Locate and identify every blood parasite.
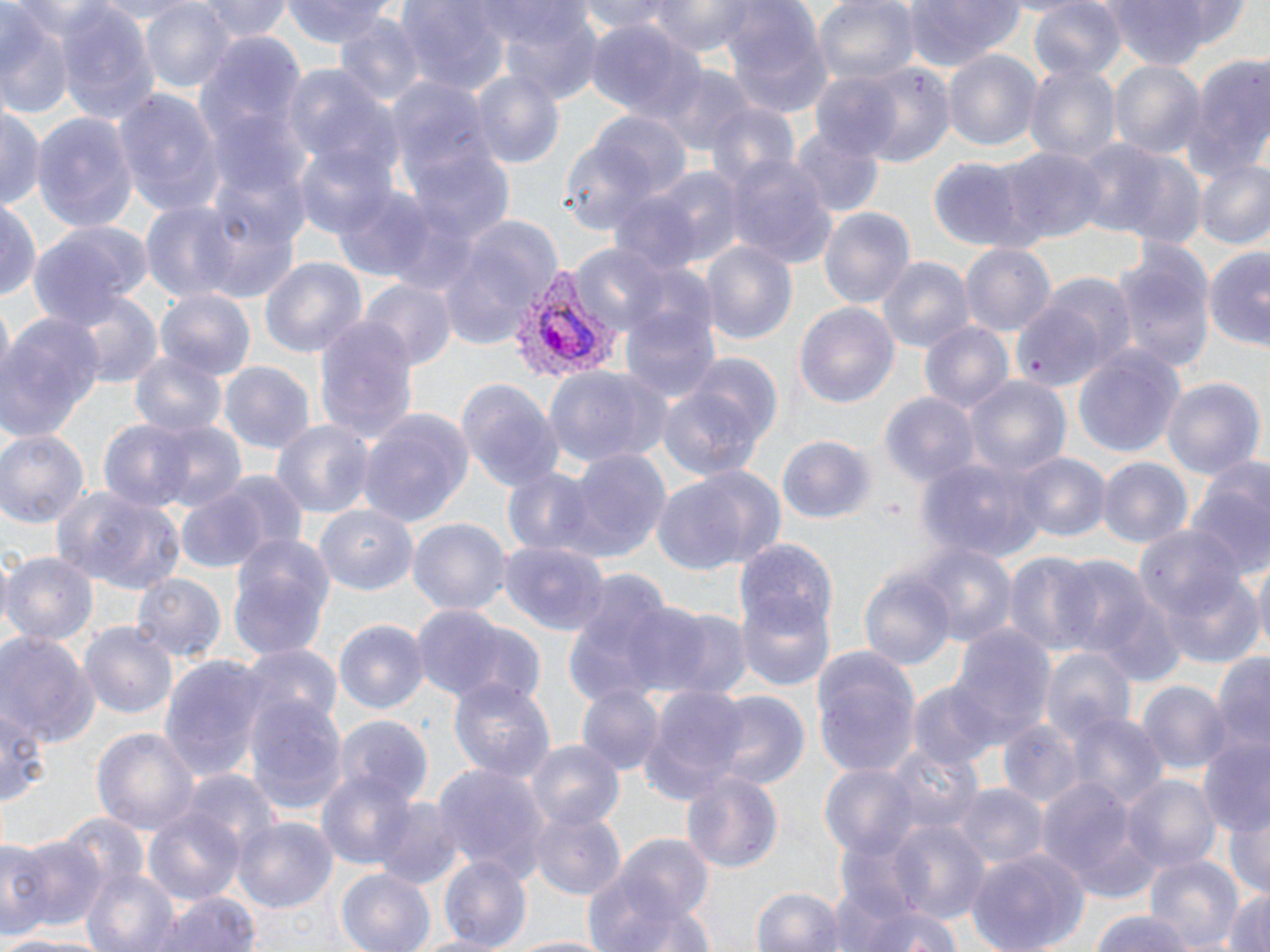

Approximate bounding boxes as named x1/y1/x2/y2 corners in pixels.
Plasmodium vivax-infected red blood cells: (x1=508, y1=266, x2=624, y2=389).
No Plasmodium falciparum, Plasmodium ovale, Plasmodium malariae, Babesia divergens, or Trypanosoma brucei observed.

slide-level diagnosis = Plasmodium vivax
uninfected red blood cell locations = approximate bounding boxes as named x1/y1/x2/y2 corners in pixels: (x1=138, y1=0, x2=231, y2=92), (x1=199, y1=0, x2=291, y2=42), (x1=283, y1=0, x2=399, y2=48), (x1=577, y1=0, x2=679, y2=36), (x1=647, y1=0, x2=761, y2=55), (x1=813, y1=0, x2=918, y2=87), (x1=898, y1=0, x2=1026, y2=70), (x1=1028, y1=1, x2=1127, y2=84), (x1=1095, y1=1, x2=1239, y2=69), (x1=401, y1=2, x2=507, y2=97), (x1=57, y1=3, x2=159, y2=127), (x1=719, y1=5, x2=832, y2=116), (x1=0, y1=7, x2=76, y2=118), (x1=496, y1=7, x2=603, y2=104), (x1=334, y1=15, x2=429, y2=104), (x1=584, y1=19, x2=702, y2=126), (x1=942, y1=49, x2=1044, y2=155), (x1=1182, y1=54, x2=1270, y2=182), (x1=1024, y1=60, x2=1120, y2=166), (x1=1108, y1=61, x2=1204, y2=161), (x1=839, y1=63, x2=957, y2=169), (x1=281, y1=65, x2=401, y2=191), (x1=656, y1=65, x2=755, y2=157), (x1=470, y1=70, x2=565, y2=173), (x1=387, y1=79, x2=493, y2=195), (x1=114, y1=88, x2=224, y2=220), (x1=703, y1=101, x2=803, y2=197), (x1=0, y1=102, x2=44, y2=214), (x1=32, y1=112, x2=139, y2=234), (x1=554, y1=120, x2=675, y2=240), (x1=790, y1=127, x2=884, y2=219), (x1=1071, y1=140, x2=1170, y2=235), (x1=996, y1=145, x2=1106, y2=245), (x1=295, y1=146, x2=395, y2=240), (x1=1097, y1=147, x2=1209, y2=249), (x1=411, y1=149, x2=515, y2=245), (x1=726, y1=157, x2=837, y2=266), (x1=928, y1=159, x2=1030, y2=249), (x1=1192, y1=159, x2=1270, y2=251), (x1=643, y1=167, x2=744, y2=269), (x1=608, y1=187, x2=711, y2=278), (x1=336, y1=189, x2=430, y2=279), (x1=190, y1=192, x2=303, y2=304), (x1=0, y1=198, x2=41, y2=307), (x1=135, y1=199, x2=250, y2=304), (x1=817, y1=206, x2=916, y2=310), (x1=440, y1=213, x2=562, y2=348), (x1=26, y1=220, x2=151, y2=323), (x1=1106, y1=240, x2=1215, y2=374), (x1=700, y1=241, x2=799, y2=350), (x1=961, y1=243, x2=1056, y2=337), (x1=1203, y1=243, x2=1270, y2=353), (x1=572, y1=244, x2=668, y2=332), (x1=877, y1=255, x2=975, y2=355), (x1=258, y1=258, x2=366, y2=363), (x1=1019, y1=271, x2=1138, y2=383), (x1=621, y1=278, x2=721, y2=404), (x1=360, y1=281, x2=455, y2=376), (x1=156, y1=291, x2=254, y2=380), (x1=70, y1=292, x2=162, y2=389), (x1=794, y1=301, x2=901, y2=412), (x1=0, y1=313, x2=105, y2=441), (x1=313, y1=315, x2=420, y2=452), (x1=918, y1=320, x2=1015, y2=419), (x1=1074, y1=344, x2=1187, y2=458), (x1=130, y1=352, x2=230, y2=440), (x1=657, y1=361, x2=780, y2=487), (x1=218, y1=362, x2=314, y2=455), (x1=543, y1=364, x2=671, y2=470), (x1=1160, y1=373, x2=1265, y2=481), (x1=962, y1=375, x2=1069, y2=481), (x1=455, y1=380, x2=564, y2=494), (x1=880, y1=393, x2=979, y2=490), (x1=357, y1=409, x2=474, y2=528), (x1=97, y1=419, x2=200, y2=515), (x1=271, y1=419, x2=373, y2=522), (x1=149, y1=421, x2=247, y2=515), (x1=0, y1=428, x2=90, y2=527), (x1=776, y1=434, x2=878, y2=529), (x1=558, y1=445, x2=672, y2=562), (x1=1010, y1=452, x2=1106, y2=543), (x1=914, y1=454, x2=1046, y2=563), (x1=1098, y1=457, x2=1192, y2=550), (x1=1185, y1=462, x2=1270, y2=583), (x1=500, y1=465, x2=602, y2=561), (x1=654, y1=467, x2=784, y2=575), (x1=217, y1=473, x2=308, y2=564), (x1=174, y1=484, x2=274, y2=574), (x1=52, y1=488, x2=185, y2=595), (x1=314, y1=505, x2=417, y2=597), (x1=408, y1=517, x2=511, y2=617), (x1=1137, y1=524, x2=1246, y2=619), (x1=226, y1=533, x2=335, y2=662), (x1=739, y1=541, x2=839, y2=644), (x1=906, y1=542, x2=1019, y2=654), (x1=501, y1=543, x2=609, y2=634), (x1=1004, y1=550, x2=1106, y2=659), (x1=0, y1=552, x2=96, y2=644), (x1=1053, y1=554, x2=1156, y2=667), (x1=1251, y1=559, x2=1270, y2=663), (x1=1154, y1=567, x2=1264, y2=669), (x1=859, y1=570, x2=957, y2=669), (x1=561, y1=571, x2=684, y2=709), (x1=134, y1=573, x2=226, y2=662), (x1=737, y1=592, x2=836, y2=694), (x1=645, y1=605, x2=753, y2=700), (x1=409, y1=606, x2=518, y2=708), (x1=332, y1=619, x2=429, y2=716), (x1=78, y1=620, x2=178, y2=721), (x1=943, y1=622, x2=1054, y2=751), (x1=0, y1=632, x2=98, y2=748), (x1=241, y1=646, x2=344, y2=737), (x1=810, y1=647, x2=920, y2=775), (x1=1040, y1=647, x2=1135, y2=745), (x1=1211, y1=650, x2=1270, y2=764), (x1=157, y1=653, x2=270, y2=788), (x1=448, y1=676, x2=556, y2=786), (x1=1137, y1=680, x2=1230, y2=775), (x1=907, y1=682, x2=997, y2=770), (x1=637, y1=685, x2=751, y2=802), (x1=578, y1=686, x2=664, y2=775), (x1=243, y1=691, x2=347, y2=817), (x1=706, y1=693, x2=810, y2=793), (x1=0, y1=697, x2=49, y2=809), (x1=1070, y1=712, x2=1167, y2=809), (x1=337, y1=716, x2=434, y2=805), (x1=998, y1=721, x2=1084, y2=809), (x1=91, y1=726, x2=199, y2=836), (x1=1197, y1=735, x2=1270, y2=838), (x1=882, y1=740, x2=982, y2=837), (x1=527, y1=741, x2=624, y2=832), (x1=311, y1=763, x2=415, y2=868), (x1=432, y1=764, x2=549, y2=879), (x1=818, y1=765, x2=920, y2=860), (x1=679, y1=768, x2=784, y2=873), (x1=183, y1=771, x2=279, y2=867), (x1=1120, y1=773, x2=1222, y2=875), (x1=1034, y1=777, x2=1142, y2=891), (x1=955, y1=784, x2=1046, y2=869), (x1=374, y1=798, x2=462, y2=890), (x1=143, y1=802, x2=248, y2=908), (x1=1227, y1=803, x2=1270, y2=903), (x1=528, y1=808, x2=627, y2=902), (x1=60, y1=812, x2=149, y2=896), (x1=233, y1=816, x2=338, y2=915), (x1=875, y1=820, x2=991, y2=922), (x1=0, y1=833, x2=46, y2=940), (x1=11, y1=834, x2=106, y2=935), (x1=602, y1=835, x2=719, y2=938), (x1=963, y1=847, x2=1088, y2=952), (x1=438, y1=853, x2=531, y2=951), (x1=1143, y1=854, x2=1242, y2=951), (x1=81, y1=867, x2=180, y2=952), (x1=336, y1=867, x2=435, y2=952), (x1=749, y1=887, x2=849, y2=952), (x1=1221, y1=887, x2=1270, y2=952), (x1=146, y1=888, x2=263, y2=952), (x1=834, y1=896, x2=961, y2=952), (x1=1089, y1=910, x2=1197, y2=952), (x1=0, y1=933, x2=90, y2=952), (x1=500, y1=934, x2=619, y2=952)
preparation = thin blood smear
modality = optical microscopy
field of view = one of a larger specimen
image size = 1270×952 pixels
stain = May-Grünwald-Giemsa
magnification = 1000x